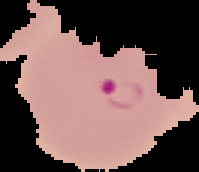

Summary:
  - Preparation: thin blood film
  - Malaria status: parasitized
  - Image size: 199×172 pixels
  - Image type: segmented cell region with the area outside set to black